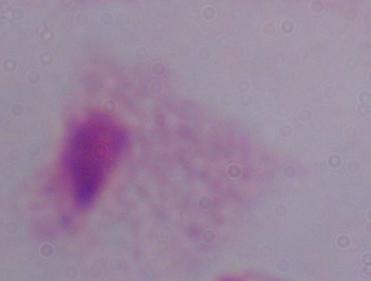
Summary:
  - Modality: micrograph
  - Identification: trichomonad
  - Magnification: 1000x